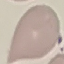
Malaria status: uninfected. Thin smear of blood. Giemsa-stained preparation. Automatically extracted cell patch, resized to 64 × 64 pixels. Acquired by smartphone through the microscope eyepiece.